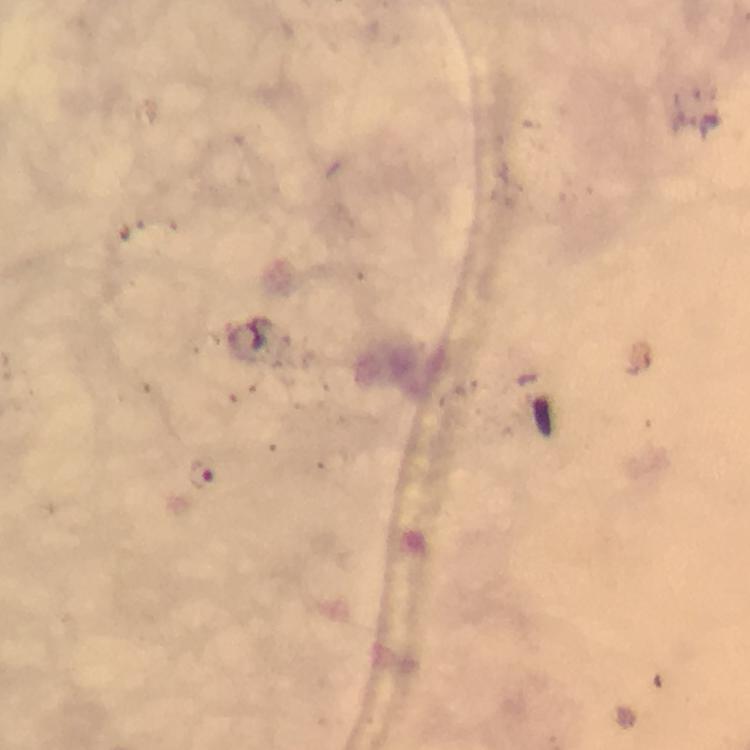
Approximate centers as {x, y} in pixels. Malaria parasite locations: {202, 476}. Smartphone photograph taken through a microscope. Immersion oil was used. 100x magnification. A crop from one field of view. Giemsa stain. Image is 750×750 pixels. Thick blood film. From a malaria diagnostic workup.